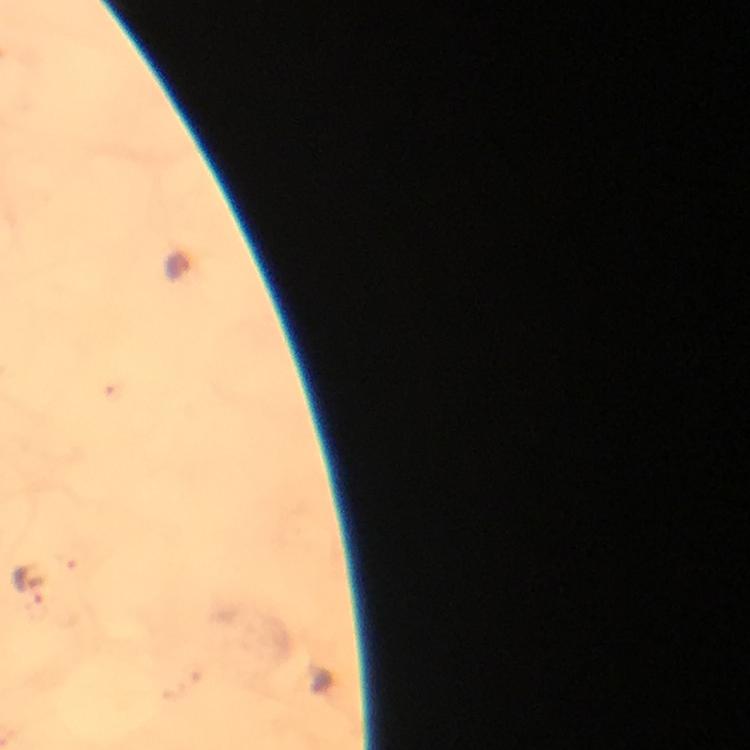
Approximate centers as [x, y] in pixels. Plasmodium parasite locations: [177, 267], [30, 583]. A crop from one field of view. Photographed with a smartphone mounted on the microscope. Immersion oil applied. 100x magnification. Thick smear. From a malaria diagnostic workup. Image is 750×750 pixels. Giemsa stain.